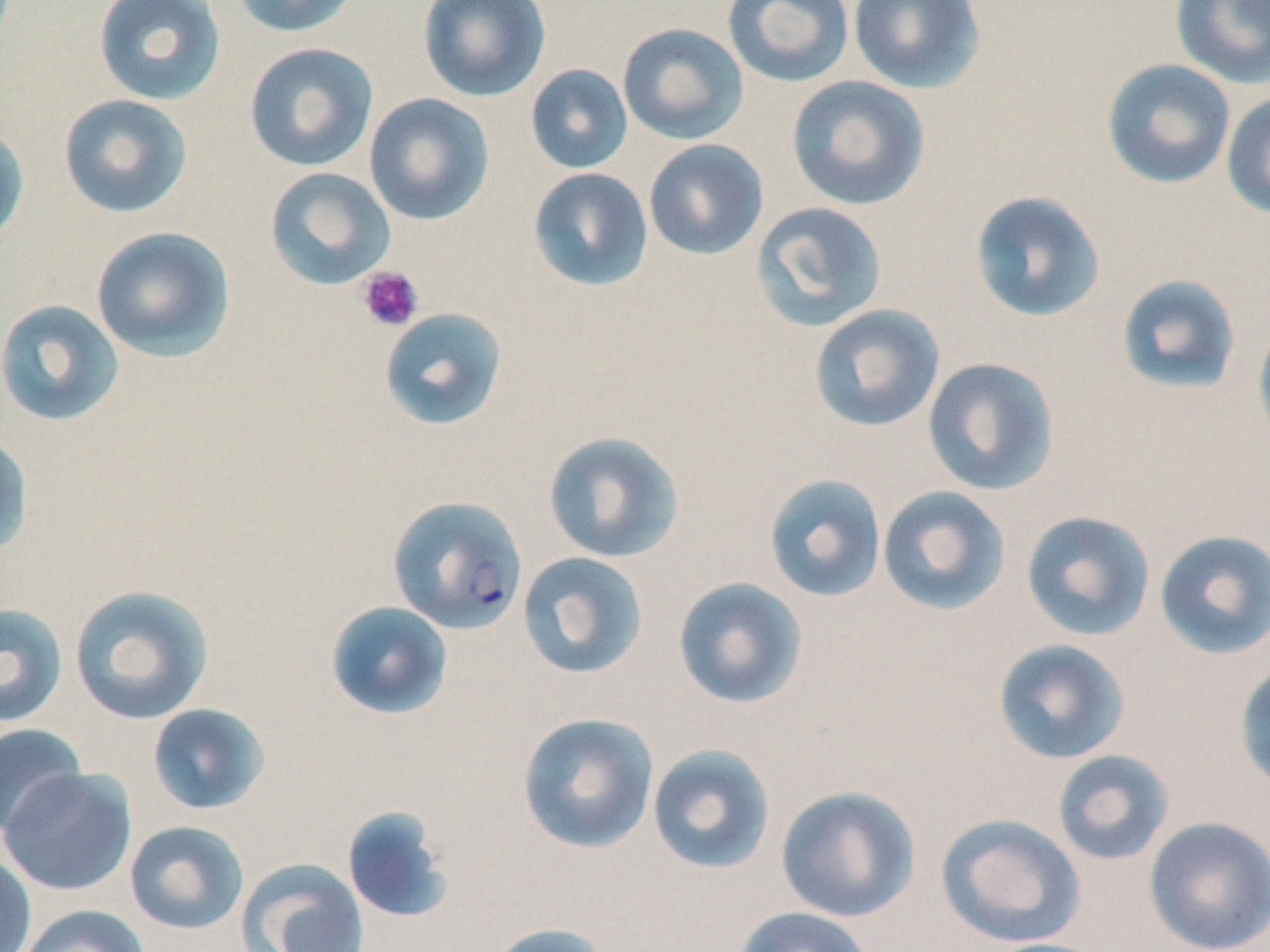

Summary:
  - Coordinate format: approximate bounding boxes as (x1,y1)-(x2,y2) corner pairs in pixels
  - Uninfected red blood cell locations: (92,0)-(226,106), (230,0)-(360,38), (417,0)-(551,102), (722,0)-(855,88), (847,0)-(986,93), (1169,0)-(1270,88), (617,22)-(748,145), (244,42)-(379,171), (1101,58)-(1236,189), (525,64)-(633,174), (786,76)-(930,211), (1221,91)-(1270,220), (58,93)-(193,218), (364,93)-(495,226), (0,123)-(30,248), (643,139)-(769,260), (264,166)-(395,290), (528,167)-(654,292), (969,190)-(1106,323), (751,201)-(887,332), (91,226)-(236,362), (1115,274)-(1242,396), (0,299)-(125,426), (808,304)-(946,433), (379,307)-(508,432), (1252,320)-(1270,450), (922,357)-(1060,496), (0,429)-(33,559), (543,431)-(685,564), (763,473)-(888,602), (876,485)-(1011,616), (1020,509)-(1156,642), (1154,529)-(1270,661), (517,551)-(649,679), (672,577)-(808,709), (68,584)-(214,725), (325,601)-(454,720), (0,602)-(68,727), (992,638)-(1131,765), (1234,660)-(1270,797), (146,703)-(272,816), (517,712)-(659,855), (0,723)-(88,838), (647,743)-(776,876), (1052,750)-(1175,866), (0,768)-(137,896), (775,785)-(921,922), (341,805)-(456,925), (935,813)-(1086,948), (1143,815)-(1270,952), (125,820)-(250,935), (0,851)-(37,952), (236,858)-(369,952), (17,904)-(150,952), (731,906)-(876,952), (488,922)-(616,952), (978,937)-(1113,952)
  - Plasmodium falciparum-infected red blood cell locations: (388,496)-(528,633)
  - Platelet locations: (357,266)-(423,332)
  - Slide-level diagnosis: Plasmodium falciparum
  - Magnification: 1000x
  - Field of view: one of a larger specimen
  - Modality: optical microscopy
  - Preparation: thin blood film
  - Image size: 1270×952 pixels
  - Stain: May-Grünwald-Giemsa